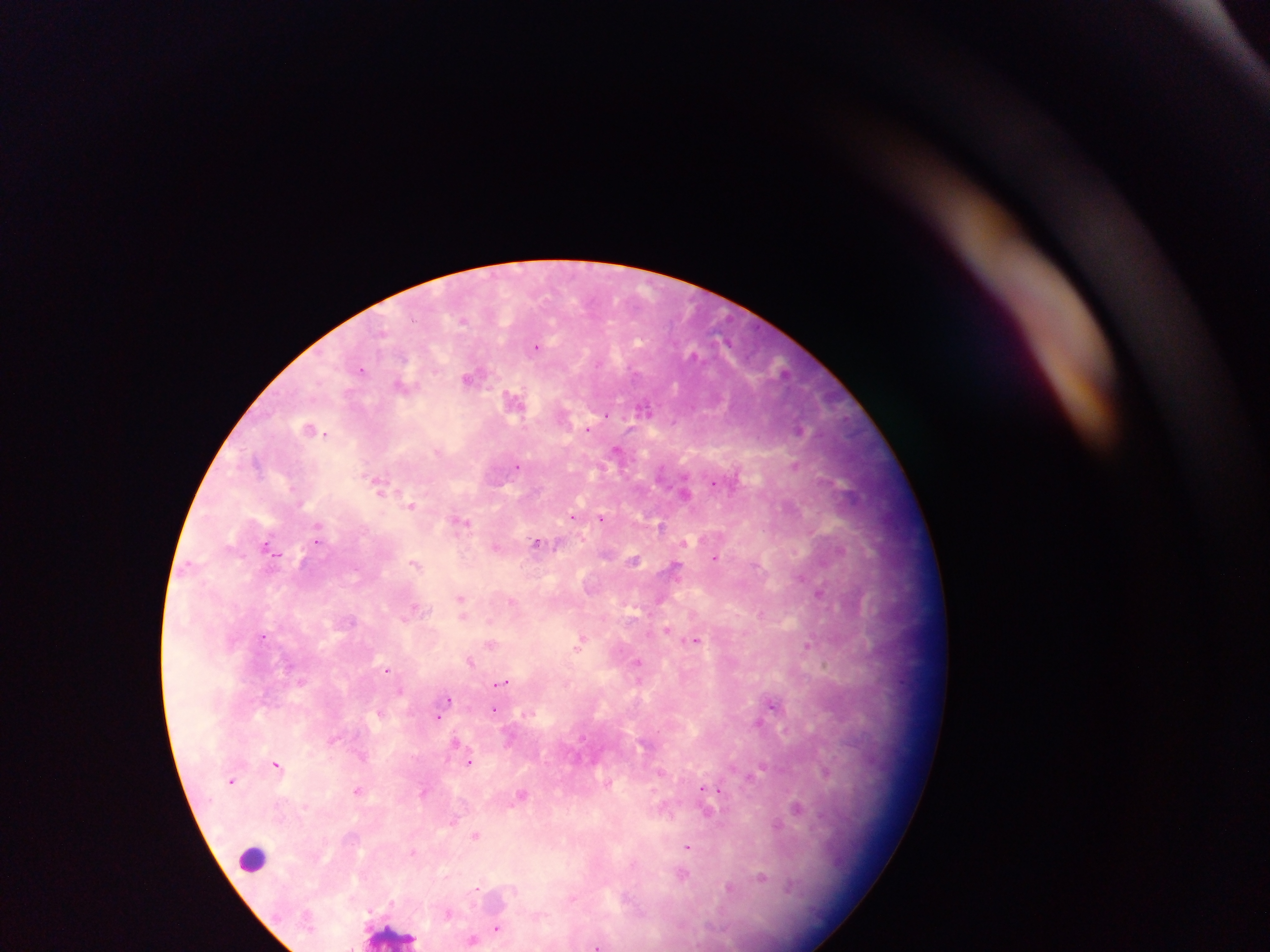

Approximate centers as [x, y] in pixels.
Summary:
  - Malaria parasite locations: [537, 345], [361, 369], [472, 377], [404, 385], [515, 400], [644, 409], [311, 428], [588, 428], [799, 429], [618, 451], [795, 463], [518, 465], [380, 484], [686, 490], [411, 505], [573, 516], [602, 518], [461, 521], [660, 525], [685, 543], [538, 544], [269, 546], [496, 546], [716, 558], [634, 559], [414, 563], [675, 568], [820, 592], [461, 600], [512, 600], [761, 613], [667, 631], [263, 636], [581, 641], [696, 641], [491, 643], [807, 646], [471, 661], [639, 663], [388, 669], [504, 682], [402, 690], [448, 700], [774, 704], [495, 708], [438, 716], [759, 723], [333, 739], [455, 742], [470, 761], [277, 764], [661, 772], [826, 772], [232, 780], [714, 788], [358, 789], [704, 789], [425, 791], [521, 794], [798, 807], [707, 811], [453, 820], [777, 825], [476, 835], [688, 846], [414, 852], [682, 875], [762, 876], [731, 888], [478, 889], [449, 912], [498, 927], [472, 939], [600, 945]
  - Leukocyte locations: [253, 859], [394, 935]
  - Field of view: single
  - Image size: 1270×952 pixels
  - Preparation: thick blood film
  - Capture: mobile-phone photograph through a microscope
  - Country: Ghana